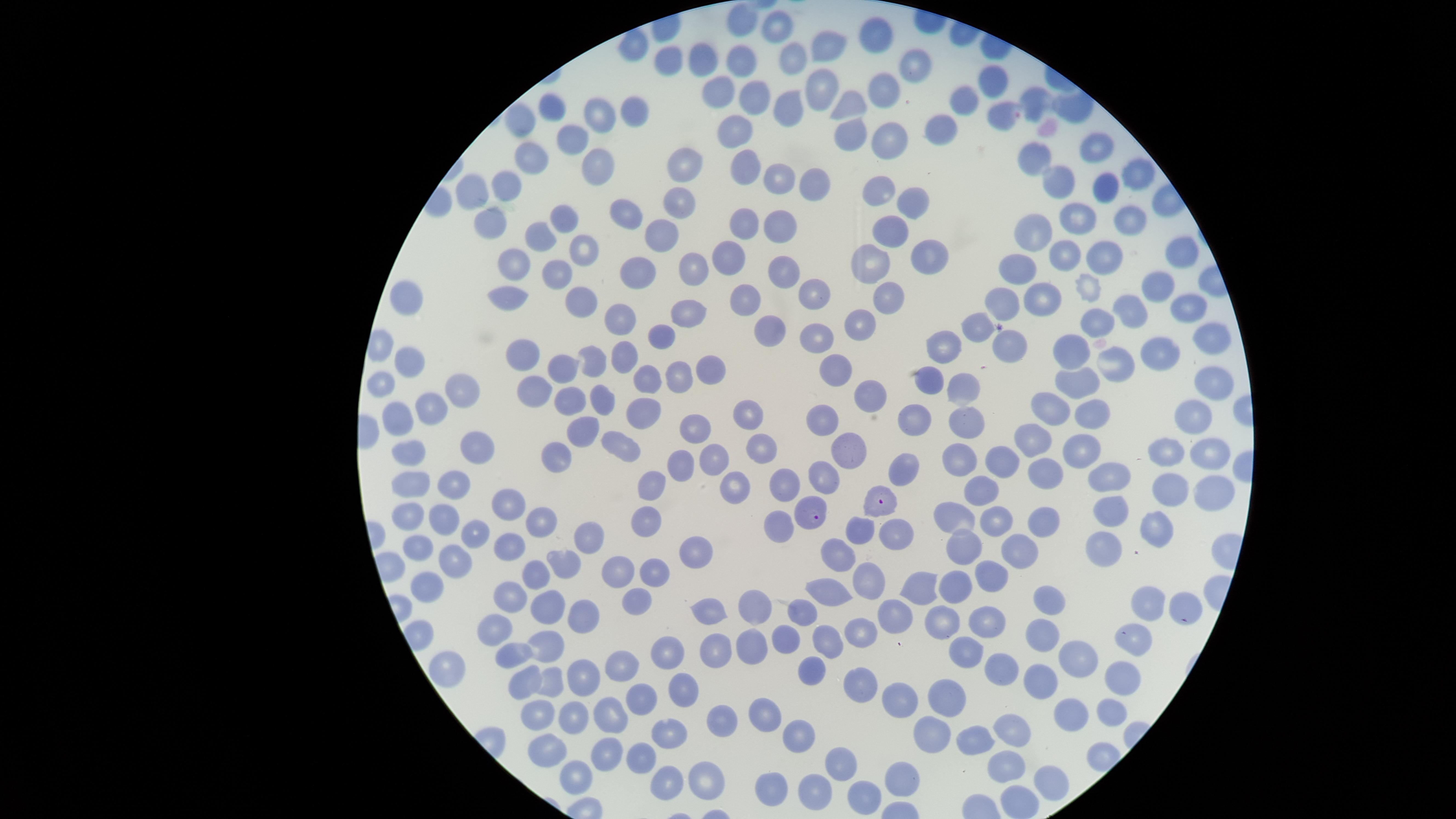

uninfected_RBCs: 'approximate marker points as [x, y] in pixels: [744, 24], [776, 28], [874, 31], [636, 43], [831, 43], [676, 54], [793, 56], [704, 58], [739, 58], [911, 62], [819, 81], [990, 81], [885, 82], [716, 93], [752, 97], [962, 99], [1036, 99], [847, 101], [554, 107], [1072, 107], [625, 110], [784, 110], [590, 114], [996, 115], [522, 118], [737, 127], [948, 129], [853, 131], [890, 133], [572, 137], [1092, 144], [1036, 155], [529, 159], [692, 168], [1138, 168], [594, 170], [746, 170], [780, 178], [811, 180], [1057, 181], [508, 184], [878, 186], [1106, 186], [476, 189], [677, 198], [912, 203], [624, 211], [1074, 214], [561, 217], [1132, 217], [750, 220], [490, 224], [778, 226], [888, 231], [655, 232], [540, 233], [1036, 233], [584, 249], [1097, 251], [931, 253], [1065, 253], [1177, 253], [874, 258], [733, 259], [517, 260], [1014, 268], [776, 269], [694, 270], [560, 271], [637, 273], [1157, 284], [1085, 291], [512, 292], [744, 295], [890, 295], [1044, 298], [816, 299], [1006, 301], [410, 302], [577, 302], [1188, 306], [1137, 310], [688, 314], [624, 316], [857, 321], [1101, 323], [982, 325], [771, 327], [657, 331], [815, 331], [1010, 342], [1209, 343], [952, 345], [1073, 349], [521, 353], [1163, 353], [624, 356], [596, 357], [1120, 357], [407, 361], [565, 368], [703, 371], [833, 374], [679, 376], [935, 376], [1079, 379], [1212, 380], [646, 381], [383, 384], [532, 386], [964, 386], [455, 392], [866, 397], [569, 400], [598, 401], [1049, 407], [638, 408], [426, 410], [394, 414], [1102, 416], [913, 417], [825, 419], [749, 420], [968, 421], [1190, 421], [698, 425], [585, 433], [1034, 433], [621, 443], [475, 445], [1168, 448], [413, 451], [762, 451], [1090, 451], [1210, 451], [845, 452], [717, 455], [557, 457], [684, 457], [960, 457], [997, 461], [1114, 472], [901, 473], [1044, 473], [412, 481], [819, 481], [986, 482], [788, 483], [455, 484], [651, 486], [1170, 487], [737, 488], [1216, 494], [509, 501], [1113, 510], [409, 511], [959, 514], [446, 515], [541, 516], [643, 517], [777, 517], [1000, 519], [1050, 521], [861, 531], [1159, 531], [472, 533], [893, 535], [591, 537], [1097, 540], [510, 541], [966, 542], [419, 544], [1018, 546], [837, 551], [695, 553], [456, 557], [560, 564], [618, 571], [653, 571], [870, 576], [535, 578], [995, 579], [960, 580], [427, 583], [927, 587], [832, 592], [514, 594], [1046, 595], [1144, 599], [631, 602], [543, 605], [800, 607], [1180, 607], [756, 608], [706, 611], [580, 614], [988, 614], [893, 616], [946, 620], [504, 629], [863, 629], [1043, 631], [786, 634], [1135, 639], [821, 640], [549, 644], [749, 648], [712, 649], [667, 655], [517, 656], [975, 656], [1083, 657], [621, 659], [1001, 668], [1126, 669], [451, 671], [809, 672], [525, 674], [582, 675], [1042, 678], [548, 684], [859, 686], [684, 687], [893, 700], [635, 701], [950, 706], [1070, 708], [1114, 709], [762, 713], [535, 715], [573, 716], [721, 716], [606, 719], [936, 724], [1015, 728], [671, 734], [977, 734], [794, 735], [544, 748], [607, 754], [641, 759], [844, 760], [1005, 765], [1050, 774], [906, 775], [571, 776], [701, 781], [774, 783], [666, 786], [866, 792], [1020, 796], [815, 798]'
species: Plasmodium falciparum
preparation: thin blood film
presence: malaria parasites seen
visible_region: circular
capture: smartphone photograph through the microscope eyepiece
stain: Giemsa
image_size: 1456×819 pixels
field_of_view: single
parasitized_RBCs: 'approximate marker points as [x, y] in pixels: [886, 504], [810, 514]'